Classify this cell by malaria status.
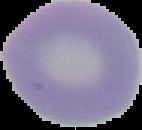
It is uninfected.

Summary:
  - Image size: 142×130 pixels
  - Preparation: thin blood film
  - Image type: segmented cell region with the area outside set to black